Assess this cell for malaria.
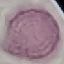

It is uninfected.

preparation = thin blood smear
image type = automatically extracted cell patch, resized to 64 × 64 pixels
stain = Giemsa
capture = smartphone camera at the microscope eyepiece